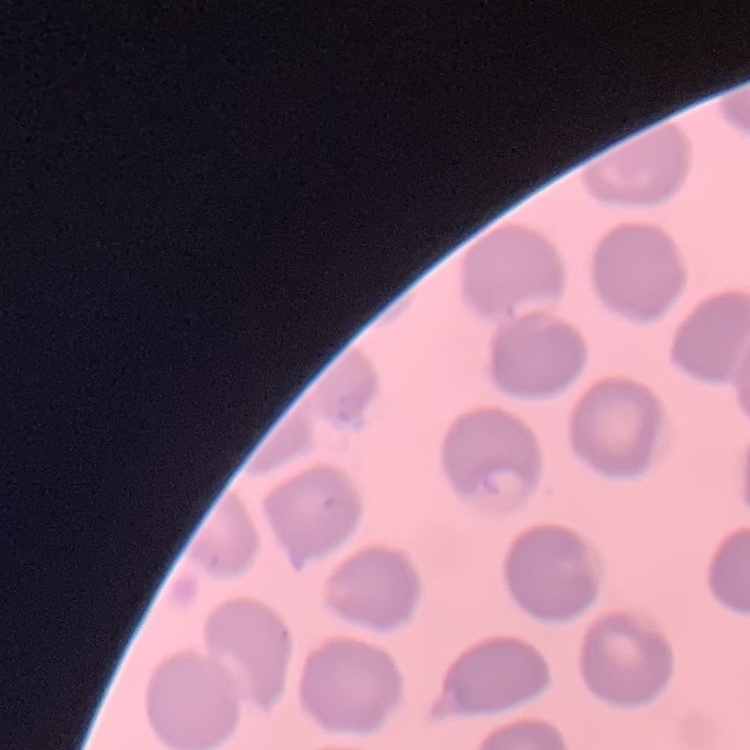

The erythrocytes exhibit no rouleaux formation. Thin blood film. Square crop of a larger photomicrograph. Stained with either Field's or Giemsa.